State which cell type is depicted.
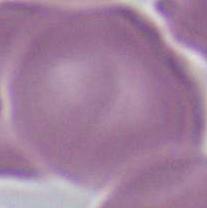
This is an erythrocyte.

{
  "modality": "micrograph",
  "magnification": "1000x"
}